Report the malaria status of this cell.
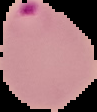
Parasitized.

Segmented cell region on a black background. Image is 97×112 pixels. From a thin blood film.